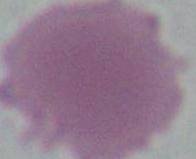

modality = micrograph
magnification = 1000x
identification = red blood cell